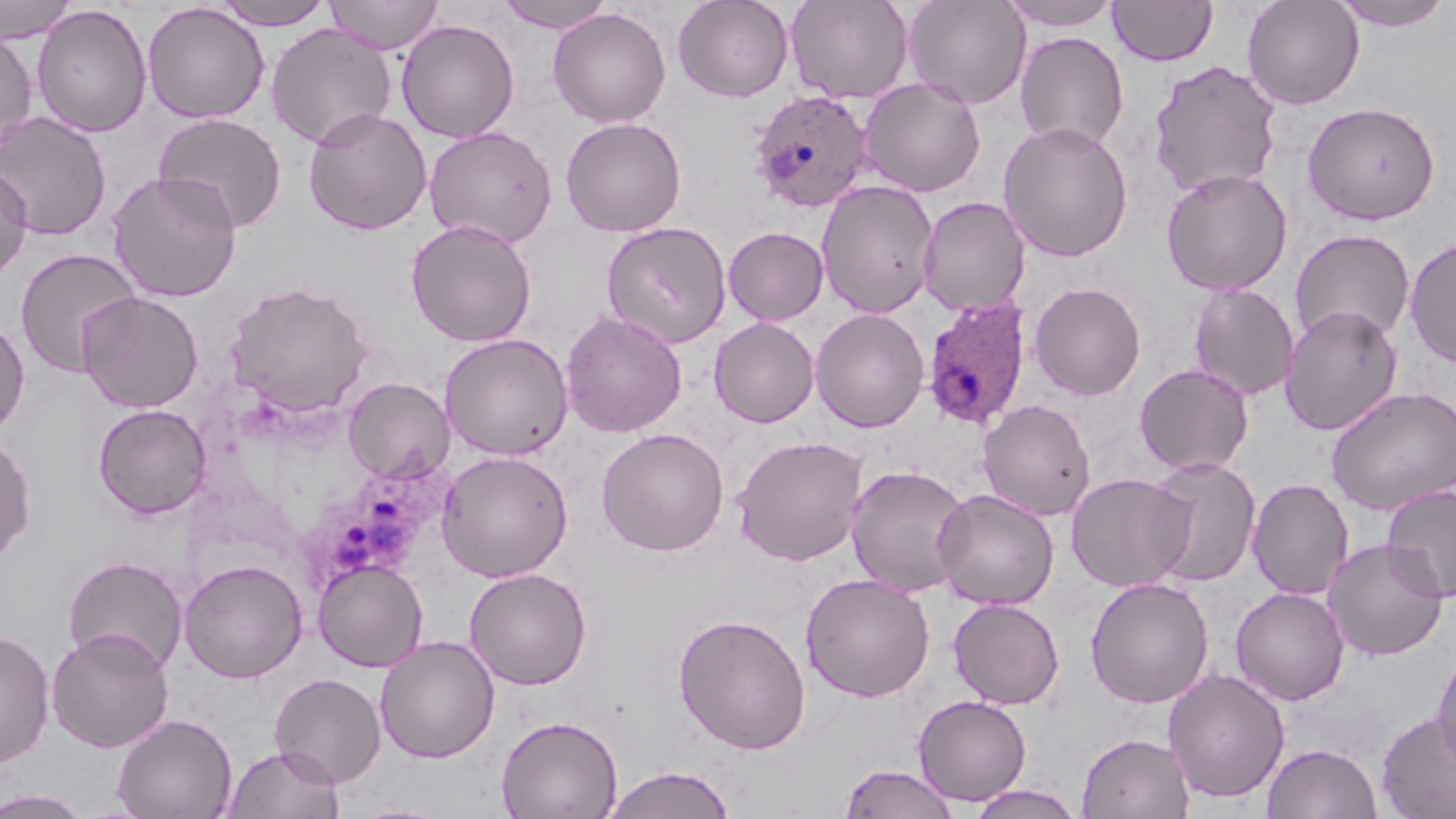
slide_level_diagnosis: Plasmodium ovale
image_size: 1456×819 pixels
preparation: thin blood smear
plasmodium_ovale_infected_red_blood_cell_locations: 'approximate bounding boxes as named x1/y1/x2/y2 corners in pixels: (x1=746, y1=89, x2=875, y2=214), (x1=921, y1=297, x2=1033, y2=431), (x1=300, y1=460, x2=447, y2=587)'
stain: May-Grünwald-Giemsa
modality: optical microscopy
field_of_view: single
uninfected_red_blood_cell_locations: 'approximate bounding boxes as named x1/y1/x2/y2 corners in pixels: (x1=212, y1=0, x2=335, y2=30), (x1=324, y1=0, x2=444, y2=54), (x1=494, y1=0, x2=617, y2=33), (x1=672, y1=0, x2=794, y2=102), (x1=785, y1=0, x2=914, y2=104), (x1=903, y1=0, x2=1032, y2=110), (x1=998, y1=0, x2=1121, y2=31), (x1=1108, y1=0, x2=1218, y2=66), (x1=1242, y1=0, x2=1365, y2=110), (x1=1331, y1=0, x2=1453, y2=30), (x1=0, y1=1, x2=77, y2=44), (x1=142, y1=3, x2=269, y2=124), (x1=31, y1=4, x2=152, y2=138), (x1=548, y1=7, x2=671, y2=128), (x1=396, y1=20, x2=519, y2=142), (x1=266, y1=23, x2=396, y2=149), (x1=0, y1=30, x2=38, y2=150), (x1=1014, y1=31, x2=1129, y2=152), (x1=1148, y1=59, x2=1282, y2=200), (x1=859, y1=76, x2=986, y2=197), (x1=1302, y1=100, x2=1440, y2=225), (x1=303, y1=108, x2=432, y2=235), (x1=0, y1=111, x2=112, y2=241), (x1=153, y1=112, x2=287, y2=232), (x1=560, y1=116, x2=687, y2=237), (x1=998, y1=121, x2=1133, y2=262), (x1=424, y1=125, x2=558, y2=249), (x1=0, y1=163, x2=33, y2=279), (x1=1161, y1=167, x2=1294, y2=295), (x1=106, y1=171, x2=242, y2=303), (x1=815, y1=180, x2=939, y2=318), (x1=918, y1=196, x2=1031, y2=316), (x1=406, y1=219, x2=537, y2=346), (x1=601, y1=221, x2=732, y2=349), (x1=723, y1=226, x2=829, y2=326), (x1=1290, y1=229, x2=1416, y2=346), (x1=1404, y1=237, x2=1456, y2=367), (x1=14, y1=248, x2=143, y2=377), (x1=226, y1=281, x2=374, y2=418), (x1=1029, y1=281, x2=1146, y2=400), (x1=1188, y1=282, x2=1300, y2=401), (x1=77, y1=291, x2=204, y2=414), (x1=1279, y1=305, x2=1403, y2=436), (x1=810, y1=308, x2=929, y2=433), (x1=561, y1=309, x2=687, y2=438), (x1=0, y1=317, x2=30, y2=436), (x1=709, y1=317, x2=819, y2=428), (x1=439, y1=332, x2=574, y2=461), (x1=1134, y1=363, x2=1254, y2=475), (x1=343, y1=377, x2=454, y2=484), (x1=1325, y1=386, x2=1456, y2=515), (x1=977, y1=399, x2=1096, y2=521), (x1=92, y1=403, x2=212, y2=520), (x1=596, y1=427, x2=730, y2=556), (x1=0, y1=435, x2=36, y2=564), (x1=732, y1=435, x2=868, y2=566), (x1=437, y1=450, x2=573, y2=582), (x1=1144, y1=456, x2=1262, y2=587), (x1=845, y1=464, x2=973, y2=597), (x1=1066, y1=472, x2=1193, y2=592), (x1=1247, y1=478, x2=1353, y2=600), (x1=1382, y1=484, x2=1456, y2=605), (x1=933, y1=488, x2=1060, y2=610), (x1=1323, y1=538, x2=1449, y2=660), (x1=62, y1=554, x2=188, y2=674), (x1=179, y1=559, x2=308, y2=683), (x1=313, y1=559, x2=428, y2=673), (x1=465, y1=568, x2=592, y2=689), (x1=800, y1=572, x2=936, y2=702), (x1=1084, y1=577, x2=1214, y2=709), (x1=1231, y1=587, x2=1350, y2=705), (x1=948, y1=597, x2=1065, y2=709), (x1=674, y1=613, x2=812, y2=754), (x1=46, y1=627, x2=175, y2=753), (x1=0, y1=629, x2=55, y2=770), (x1=375, y1=635, x2=500, y2=763), (x1=1432, y1=648, x2=1456, y2=773), (x1=1163, y1=668, x2=1290, y2=804), (x1=269, y1=672, x2=387, y2=788), (x1=913, y1=695, x2=1032, y2=806), (x1=1376, y1=711, x2=1456, y2=819), (x1=112, y1=713, x2=237, y2=819), (x1=496, y1=715, x2=622, y2=819), (x1=1077, y1=732, x2=1195, y2=818), (x1=1262, y1=743, x2=1383, y2=818), (x1=223, y1=744, x2=345, y2=819), (x1=839, y1=764, x2=960, y2=819), (x1=601, y1=766, x2=737, y2=819), (x1=963, y1=784, x2=1087, y2=819), (x1=1, y1=788, x2=93, y2=818)'
magnification: 1000x